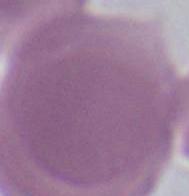
magnification: 1000x
identification: erythrocyte
modality: micrograph